Name the blood parasite species.
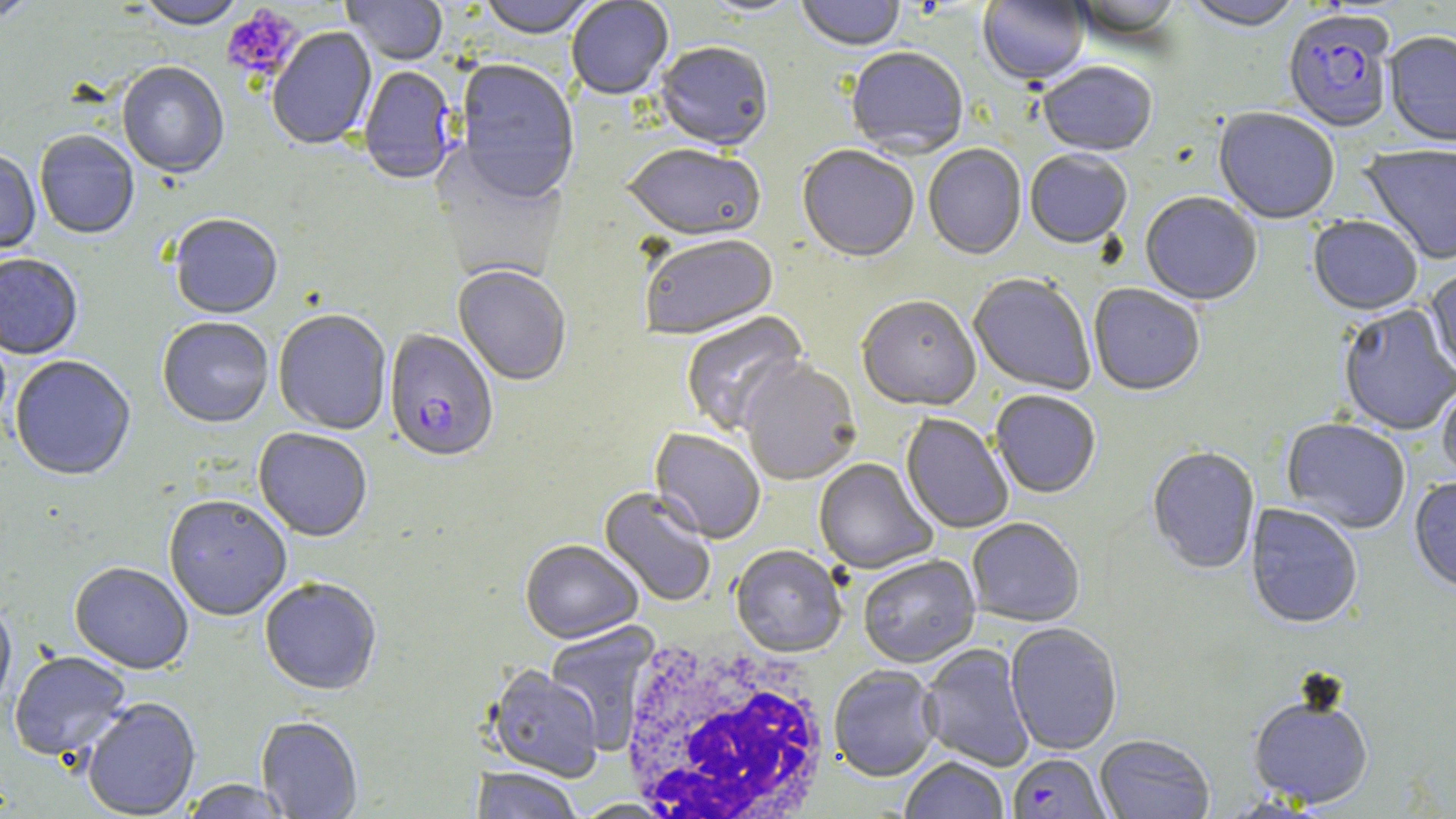

Plasmodium falciparum.

Approximate bounding boxes as (x1,y1)-(x2,y2) corner pairs in pixels. Plasmodium falciparum-infected red blood cell locations: (1282,12)-(1397,134), (359,68)-(458,186), (384,330)-(499,466), (1011,757)-(1115,819). White blood cell locations: (616,637)-(835,819). Uninfected red blood cell locations: (0,0)-(39,24), (341,0)-(448,67), (477,0)-(599,41), (566,0)-(674,101), (700,0)-(804,19), (797,0)-(906,54), (978,0)-(1091,89), (1070,0)-(1183,43), (135,1)-(247,32), (1183,1)-(1304,33), (267,27)-(377,152), (1384,33)-(1456,148), (654,43)-(774,153), (846,49)-(968,160), (453,61)-(581,207), (117,63)-(229,181), (1037,63)-(1157,159), (1213,109)-(1340,226), (34,132)-(139,241), (621,145)-(766,244), (923,145)-(1026,261), (1360,146)-(1456,265), (797,147)-(919,265), (0,150)-(41,256), (1025,152)-(1132,251), (1140,193)-(1262,307), (169,216)-(283,321), (1307,217)-(1422,317), (639,236)-(779,342), (0,256)-(83,361), (452,267)-(571,387), (1424,268)-(1456,378), (968,275)-(1095,396), (1088,285)-(1205,397), (857,298)-(981,414), (1338,305)-(1456,437), (273,311)-(392,436), (681,312)-(809,437), (157,319)-(274,430), (10,357)-(136,483), (740,361)-(861,488), (1437,382)-(1456,484), (990,392)-(1101,500), (900,414)-(1014,534), (1281,419)-(1410,535), (253,429)-(372,543), (649,429)-(765,545), (1147,448)-(1260,576), (813,458)-(938,575), (1409,479)-(1456,596), (597,488)-(716,607), (163,497)-(292,623), (1245,504)-(1362,631), (967,520)-(1085,628), (520,542)-(643,646), (730,546)-(847,659), (858,556)-(980,669), (69,563)-(193,676), (260,580)-(382,698), (0,602)-(16,715), (545,621)-(661,753), (1006,624)-(1122,756), (918,644)-(1035,772), (9,652)-(132,764), (485,667)-(603,783), (828,667)-(942,783), (1248,696)-(1374,810), (81,699)-(201,818), (255,717)-(363,818), (1091,734)-(1212,818), (900,758)-(1009,819), (471,769)-(583,819), (179,780)-(294,818). Platelet locations: (222,4)-(304,81). Thin blood smear. 1000x magnification. May-Grünwald-Giemsa stain. Optical microscopy. Image is 1456×819 pixels. One field of a larger specimen.